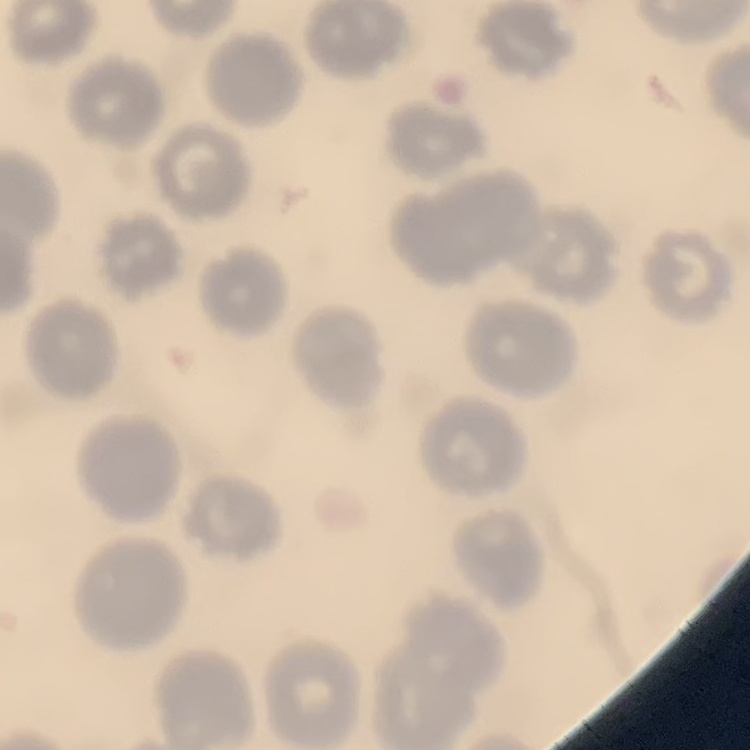 The red blood cells show no rouleaux formation. Field's or Giemsa stain. One tile cut from a larger photomicrograph. Thin blood smear.